Locate every blood parasite and identify its species.
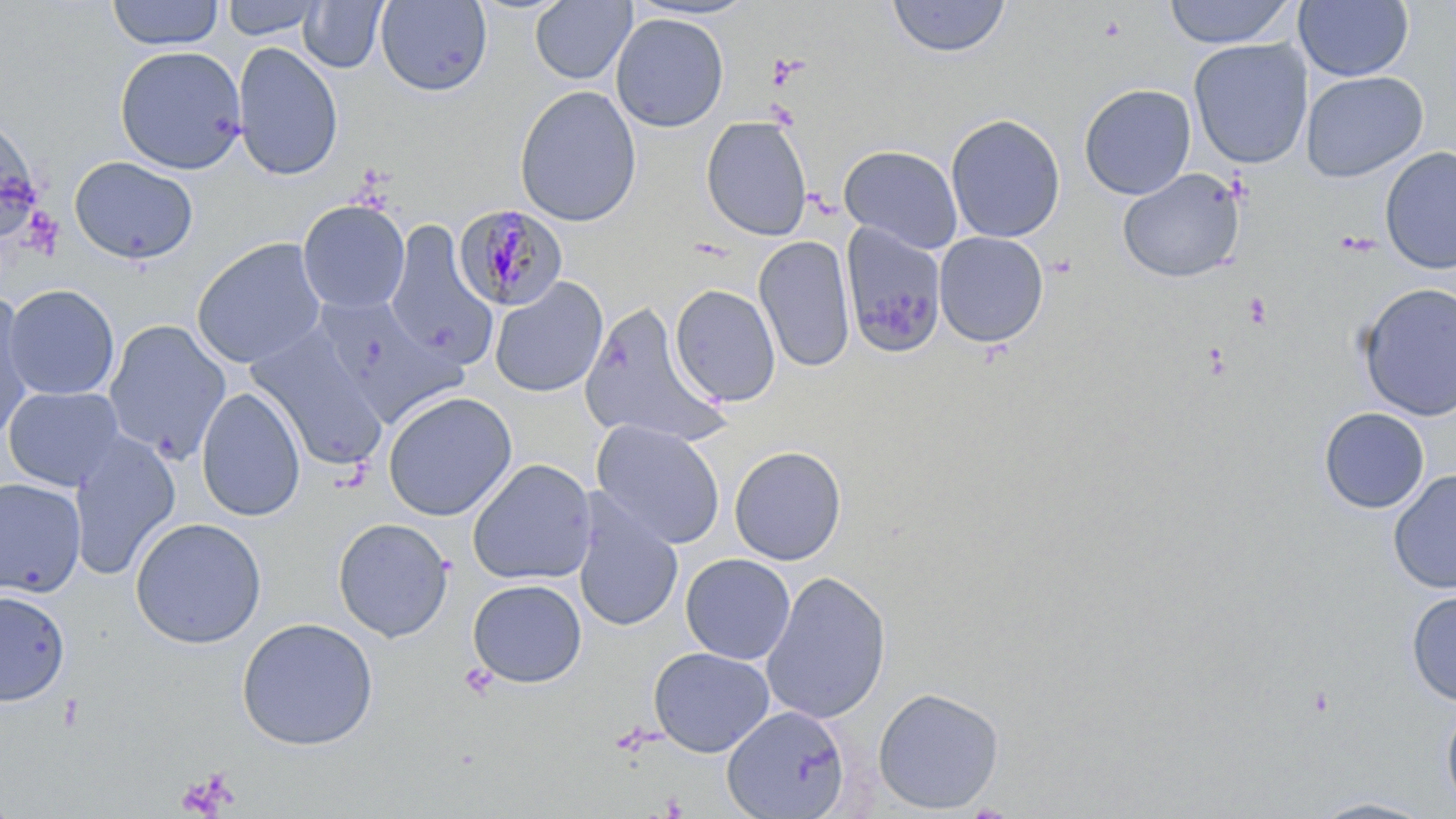
Approximate bounding boxes as named x1/y1/x2/y2 corners in pixels.
Plasmodium malariae-infected red blood cells: (x1=452, y1=203, x2=569, y2=312).
No Plasmodium falciparum, Plasmodium ovale, Plasmodium vivax, Babesia divergens, or Trypanosoma brucei observed.

Uninfected red blood cell locations: (x1=106, y1=0, x2=224, y2=50), (x1=220, y1=0, x2=325, y2=40), (x1=530, y1=0, x2=636, y2=85), (x1=887, y1=0, x2=1011, y2=60), (x1=1163, y1=0, x2=1296, y2=49), (x1=299, y1=1, x2=388, y2=73), (x1=376, y1=1, x2=492, y2=96), (x1=1293, y1=1, x2=1414, y2=82), (x1=611, y1=13, x2=729, y2=132), (x1=1188, y1=38, x2=1313, y2=169), (x1=232, y1=41, x2=344, y2=181), (x1=114, y1=45, x2=247, y2=174), (x1=1300, y1=71, x2=1428, y2=183), (x1=1079, y1=83, x2=1196, y2=200), (x1=514, y1=85, x2=642, y2=227), (x1=945, y1=113, x2=1066, y2=243), (x1=0, y1=114, x2=42, y2=246), (x1=700, y1=115, x2=813, y2=240), (x1=839, y1=145, x2=963, y2=254), (x1=1380, y1=146, x2=1456, y2=274), (x1=69, y1=155, x2=199, y2=265), (x1=1118, y1=168, x2=1246, y2=283), (x1=297, y1=200, x2=410, y2=314), (x1=384, y1=221, x2=498, y2=368), (x1=841, y1=223, x2=946, y2=357), (x1=933, y1=231, x2=1049, y2=348), (x1=753, y1=235, x2=856, y2=373), (x1=191, y1=237, x2=327, y2=369), (x1=489, y1=277, x2=608, y2=398), (x1=3, y1=283, x2=120, y2=400), (x1=1357, y1=283, x2=1456, y2=421), (x1=669, y1=284, x2=781, y2=407), (x1=0, y1=294, x2=36, y2=440), (x1=314, y1=295, x2=465, y2=424), (x1=579, y1=302, x2=727, y2=448), (x1=103, y1=319, x2=231, y2=464), (x1=249, y1=329, x2=388, y2=472), (x1=3, y1=385, x2=125, y2=491), (x1=195, y1=386, x2=306, y2=522), (x1=382, y1=390, x2=517, y2=521), (x1=1319, y1=407, x2=1430, y2=513), (x1=591, y1=420, x2=726, y2=548), (x1=68, y1=432, x2=180, y2=580), (x1=728, y1=445, x2=847, y2=566), (x1=467, y1=459, x2=597, y2=586), (x1=1389, y1=470, x2=1456, y2=595), (x1=0, y1=477, x2=86, y2=597), (x1=573, y1=496, x2=684, y2=633), (x1=129, y1=516, x2=267, y2=649), (x1=332, y1=517, x2=454, y2=642), (x1=680, y1=553, x2=795, y2=664), (x1=761, y1=570, x2=891, y2=724), (x1=466, y1=579, x2=587, y2=688), (x1=0, y1=589, x2=71, y2=706), (x1=1406, y1=590, x2=1456, y2=705), (x1=236, y1=617, x2=379, y2=750), (x1=648, y1=646, x2=775, y2=757), (x1=873, y1=686, x2=1005, y2=814), (x1=1440, y1=701, x2=1456, y2=813), (x1=722, y1=705, x2=851, y2=818), (x1=1309, y1=796, x2=1437, y2=818). Platelet locations: (x1=1243, y1=293, x2=1272, y2=328), (x1=1203, y1=341, x2=1230, y2=380), (x1=460, y1=662, x2=498, y2=699), (x1=175, y1=770, x2=238, y2=817). Slide-level diagnosis: Plasmodium malariae. Light microscopy. 1000x magnification. Image is 1456×819 pixels. May-Grünwald-Giemsa-stained preparation. Thin blood film. Single field of view.